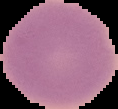
preparation = thin blood film
image type = segmented cell region with the area outside set to black
image size = 118×109 pixels
result = negative for Plasmodium parasites